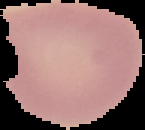

{
  "image_size": "145×130 pixels",
  "image_type": "segmented cell region with the area outside set to black",
  "preparation": "thin blood film",
  "result": "negative for malaria parasites"
}